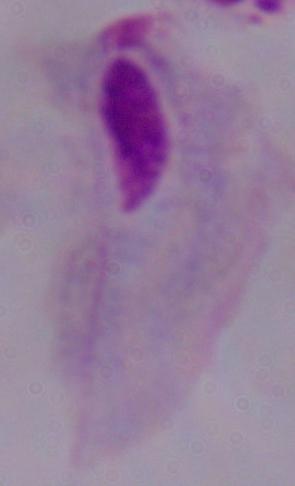
Micrograph. A trichomonad is seen. 1000x magnification.